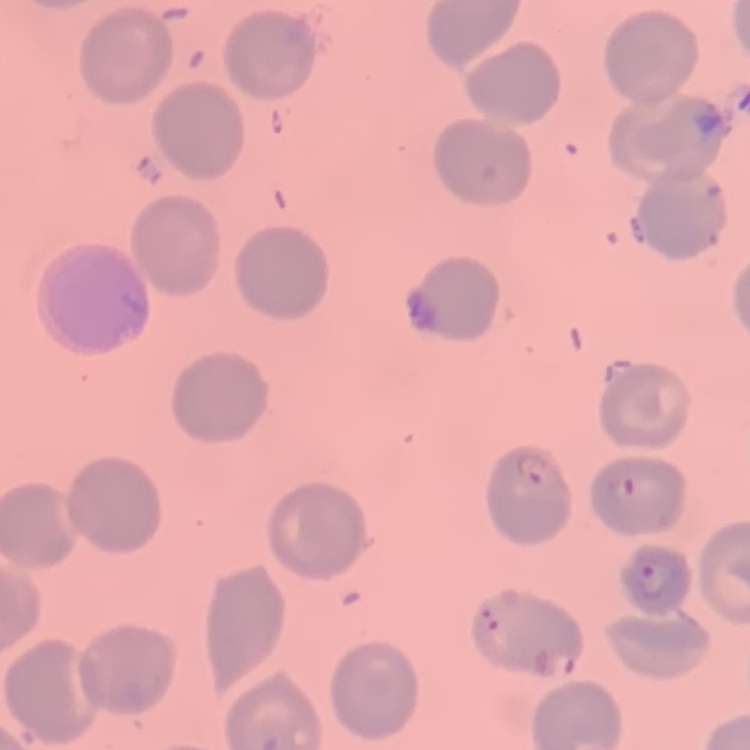 The red blood cells show no rouleaux formation. Square crop of a larger photomicrograph. Thin peripheral smear. Field's or Giemsa stain.